Describe the morphology of the erythrocytes.
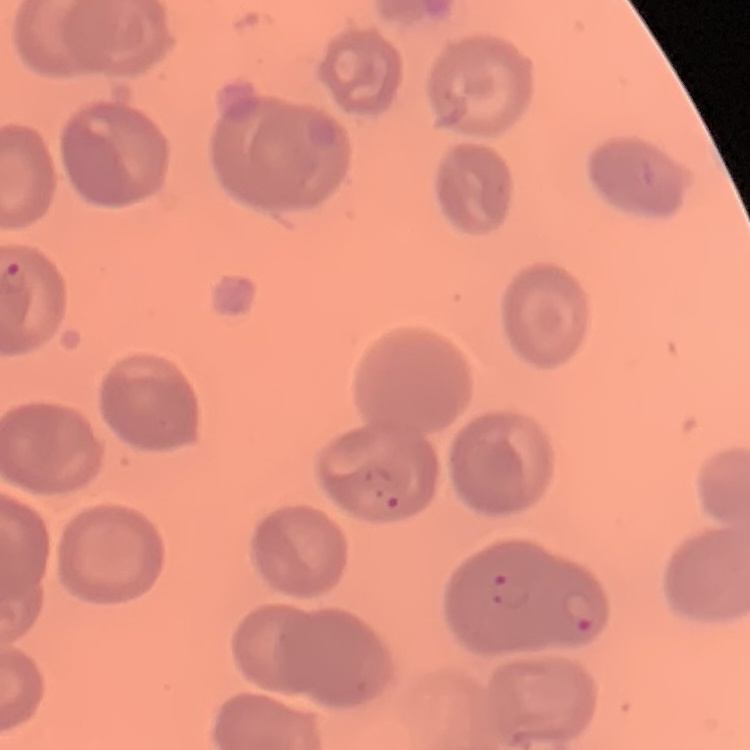

No rouleaux formation.

Summary:
  - Preparation: thin blood film
  - Image type: square crop of a larger photomicrograph
  - Stain: Field's or Giemsa